Mark where platelets are.
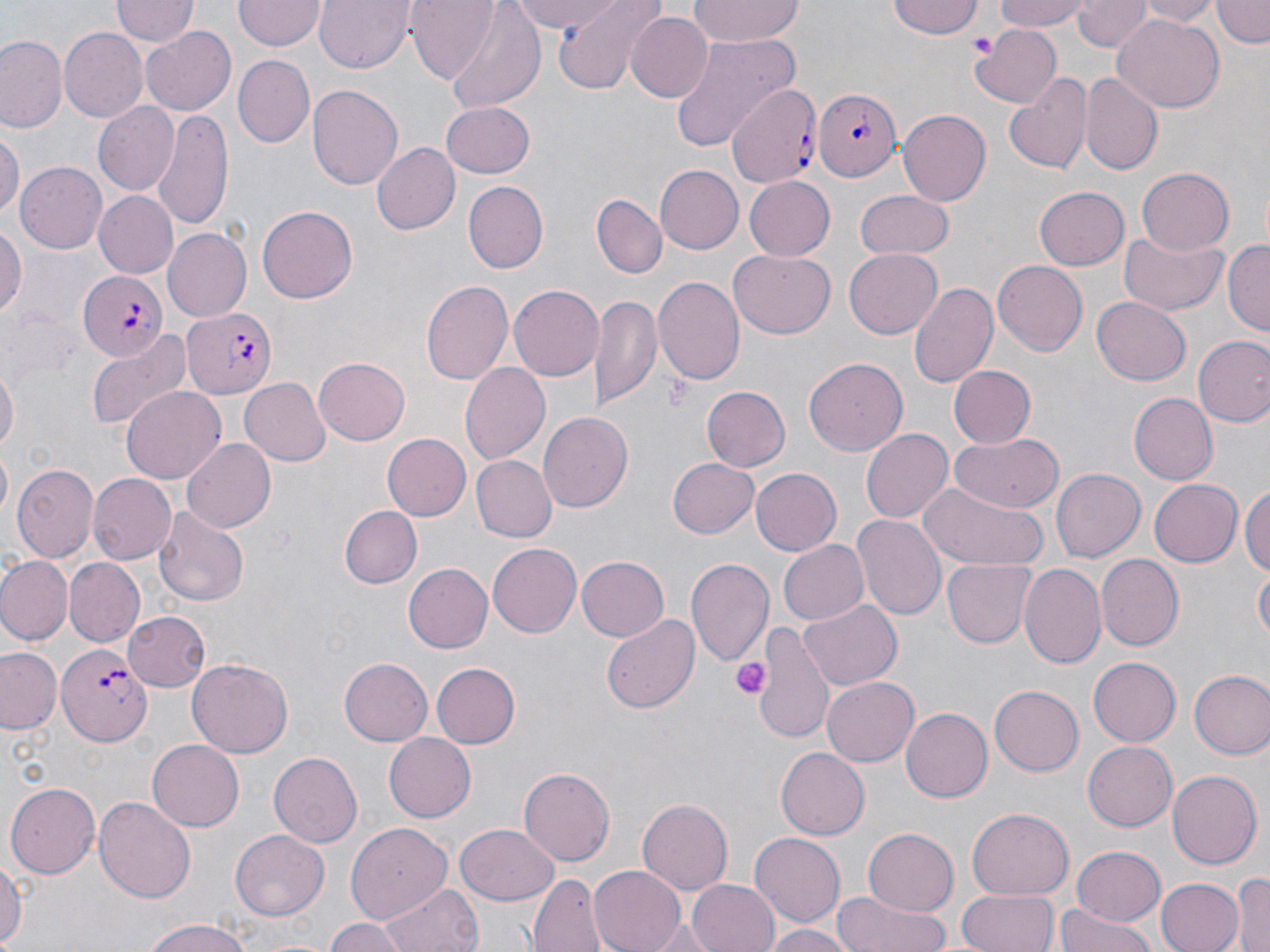

Approximate bounding boxes as (x1, y1, x2, y2) in pixels.
Platelets: (969, 29, 995, 58), (665, 372, 694, 411), (731, 657, 771, 700).

Uninfected red blood cell locations: (234, 0, 323, 53), (316, 0, 415, 73), (407, 0, 500, 83), (510, 0, 627, 34), (550, 0, 665, 94), (688, 0, 804, 45), (886, 0, 985, 41), (994, 0, 1094, 32), (1137, 0, 1219, 25), (1212, 0, 1268, 48), (110, 1, 196, 47), (1074, 1, 1148, 52), (441, 3, 546, 112), (1110, 10, 1224, 111), (626, 11, 713, 103), (58, 27, 147, 122), (140, 27, 239, 115), (971, 27, 1060, 108), (669, 33, 800, 154), (1, 35, 67, 135), (234, 56, 314, 147), (1080, 73, 1162, 176), (1006, 74, 1093, 175), (307, 83, 404, 193), (91, 102, 178, 198), (440, 102, 534, 179), (897, 107, 990, 202), (154, 109, 234, 229), (0, 127, 22, 219), (371, 141, 459, 236), (16, 161, 109, 255), (656, 166, 743, 253), (1136, 167, 1233, 255), (742, 176, 836, 261), (464, 181, 549, 271), (1033, 184, 1130, 272), (93, 191, 178, 279), (853, 192, 954, 260), (592, 194, 666, 277), (257, 205, 358, 304), (0, 220, 26, 318), (164, 227, 253, 323), (1121, 229, 1229, 316), (1223, 240, 1269, 336), (845, 248, 943, 339), (729, 250, 836, 339), (992, 260, 1087, 356), (655, 274, 744, 383), (421, 279, 514, 386), (909, 281, 998, 389), (508, 284, 604, 380), (589, 292, 661, 412), (1092, 295, 1191, 384), (85, 329, 192, 431), (1193, 335, 1270, 427), (313, 356, 409, 444), (803, 358, 910, 458), (459, 362, 550, 464), (1, 363, 18, 461), (947, 365, 1035, 450), (240, 377, 333, 465), (121, 385, 226, 485), (701, 386, 789, 471), (1128, 392, 1219, 485), (539, 411, 633, 513), (862, 427, 954, 524), (950, 432, 1061, 513), (383, 433, 472, 521), (181, 439, 276, 534), (471, 455, 556, 542), (664, 456, 759, 540), (12, 465, 98, 564), (751, 468, 842, 555), (1051, 468, 1144, 563), (88, 472, 176, 566), (1149, 476, 1243, 565), (1243, 482, 1270, 581), (918, 483, 1047, 573), (153, 502, 249, 607), (339, 505, 423, 588), (853, 513, 945, 622), (777, 540, 869, 626), (486, 543, 582, 638), (576, 554, 670, 641), (1094, 554, 1183, 651), (0, 555, 72, 645), (687, 556, 776, 667), (63, 557, 144, 646), (943, 559, 1035, 648), (1019, 563, 1107, 668), (404, 564, 493, 652), (1254, 565, 1269, 644), (799, 599, 901, 690), (123, 611, 210, 692), (601, 611, 701, 714), (753, 622, 833, 745), (0, 646, 63, 733), (1089, 657, 1181, 745), (187, 658, 293, 757), (339, 658, 433, 744), (430, 661, 520, 750), (1188, 670, 1270, 759), (822, 675, 920, 766), (990, 685, 1084, 775), (901, 706, 992, 802), (384, 734, 476, 820), (147, 740, 243, 832), (1083, 741, 1178, 830), (774, 747, 868, 840), (269, 751, 365, 845), (516, 768, 613, 866), (1167, 771, 1260, 870), (6, 780, 101, 878), (94, 796, 195, 904), (637, 797, 733, 893), (965, 808, 1073, 900), (344, 822, 453, 926), (455, 824, 560, 906), (863, 829, 958, 917), (231, 830, 328, 920), (751, 832, 845, 926), (1071, 845, 1166, 927), (0, 850, 24, 952), (588, 864, 689, 952), (1231, 868, 1270, 952), (528, 873, 607, 952), (1154, 877, 1245, 952), (686, 878, 780, 952), (383, 882, 483, 952), (957, 887, 1058, 952), (836, 892, 950, 952), (1055, 901, 1157, 952), (646, 914, 716, 951), (138, 916, 254, 952), (324, 918, 410, 951), (761, 923, 853, 952). Plasmodium falciparum-infected red blood cell locations: (727, 82, 820, 193), (815, 87, 903, 180), (76, 268, 166, 361), (185, 305, 276, 399), (57, 643, 150, 747). Slide-level diagnosis: Plasmodium falciparum. May-Grünwald-Giemsa stain. Image is 1270×952 pixels. Single field of view. Thin blood smear. Captured at 1000x magnification. Optical microscopy.